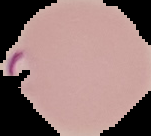
Image is 151×136 pixels. Cell region segmented out of the field of view; the surrounding area is masked to black. Result: Plasmodium parasites identified. From a thin blood smear.